Comment on the morphology of the erythrocytes.
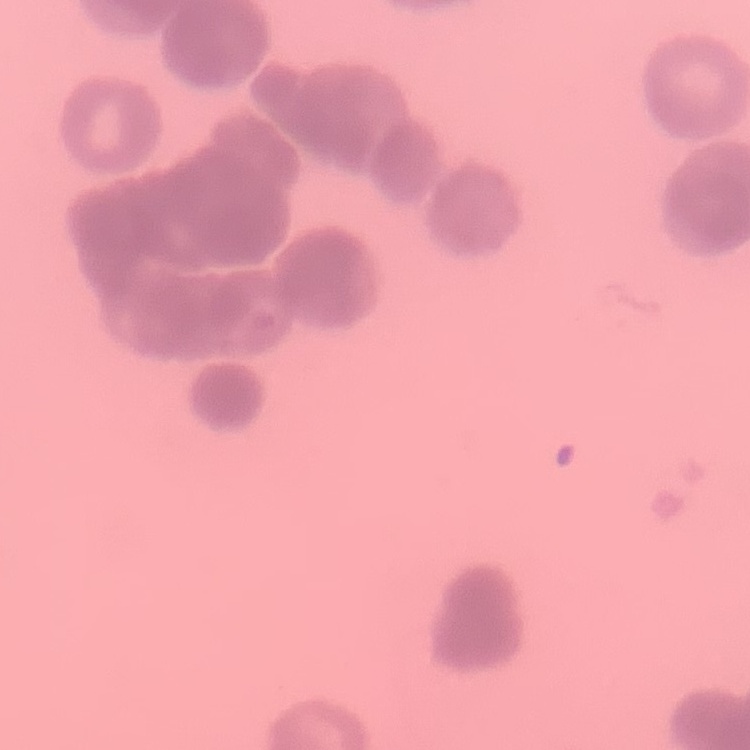
Rouleaux formation.

Thin peripheral smear. Square crop of a larger photomicrograph. Stained with either Field's or Giemsa.